Comment on the morphology of the red blood cells.
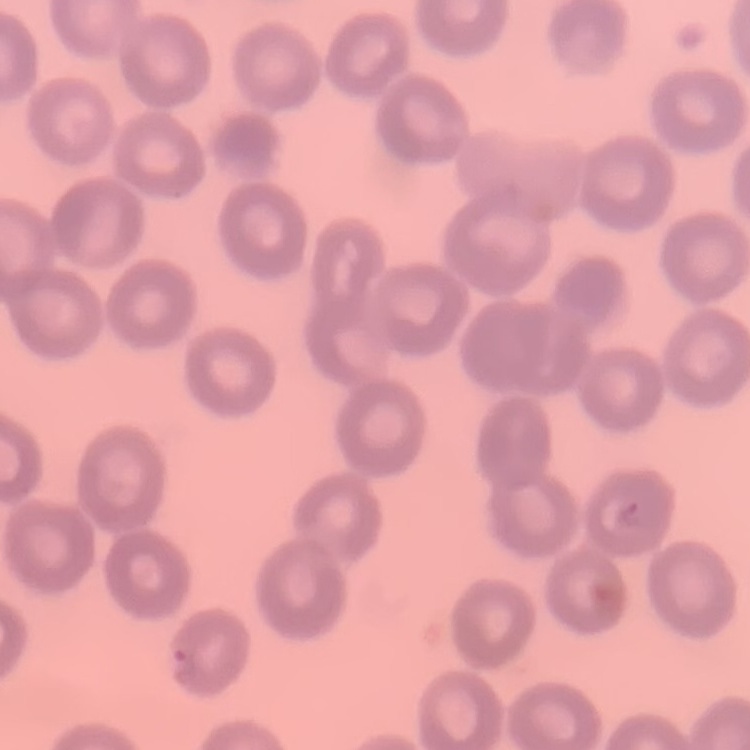

They show no rouleaux formation.

Thin blood smear. Stained with either Field's or Giemsa. Square crop of a larger photomicrograph.